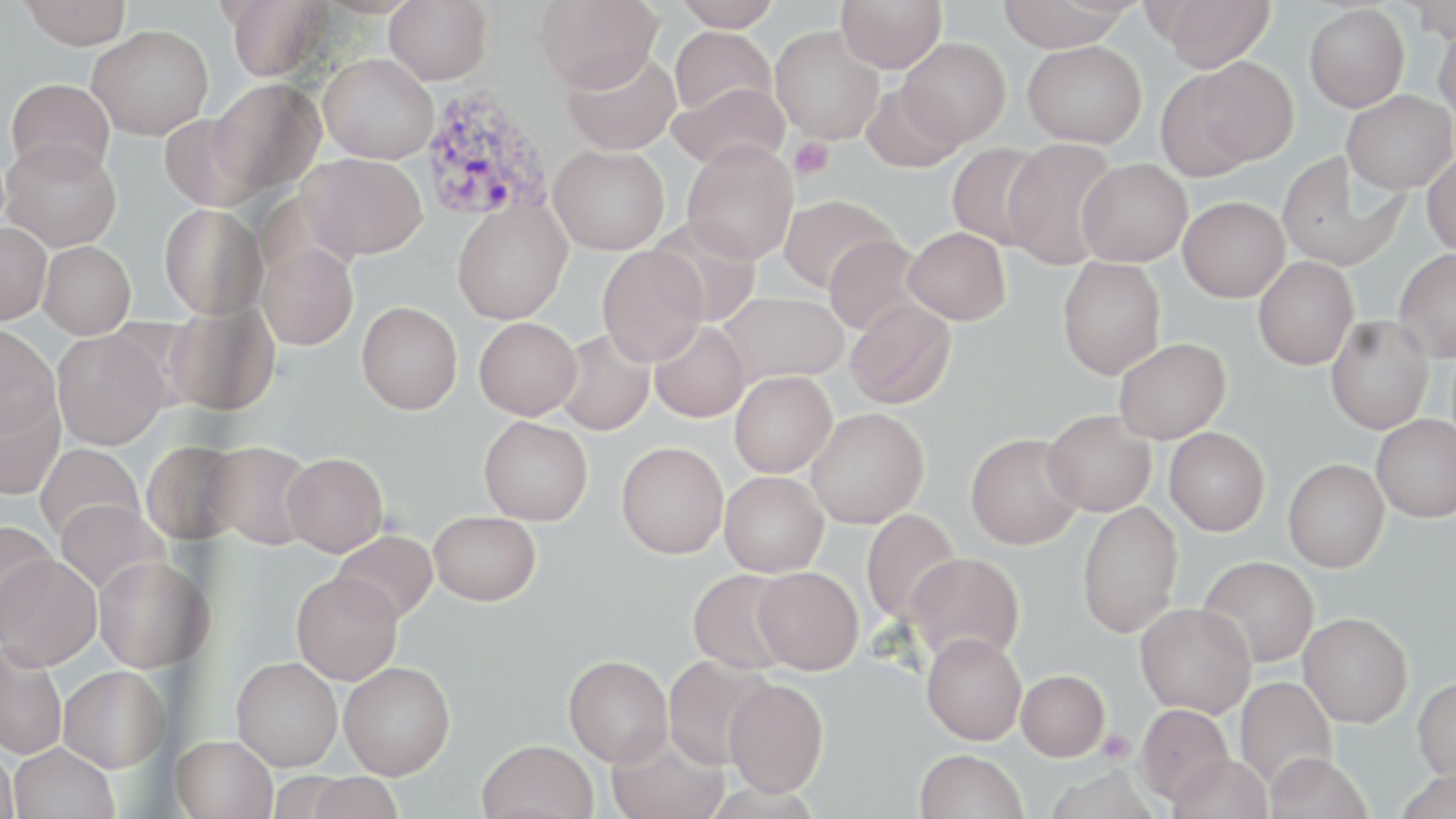
Summary:
  - Coordinate format: approximate bounding boxes as (x1,y1)-(x2,y2) corner pairs in pixels
  - Platelet locations: (788,138)-(834,179), (1097,730)-(1134,763)
  - Plasmodium vivax-infected red blood cell locations: (418,85)-(554,226)
  - Uninfected red blood cell locations: (20,0)-(133,49), (385,0)-(493,84), (534,0)-(662,93), (674,0)-(780,30), (836,0)-(946,73), (997,0)-(1132,52), (1157,0)-(1276,72), (1407,0)-(1456,42), (223,1)-(330,81), (1304,4)-(1409,111), (1434,22)-(1456,122), (87,25)-(213,139), (670,26)-(777,118), (770,26)-(884,145), (899,38)-(1011,146), (1023,40)-(1146,147), (562,49)-(681,155), (319,53)-(438,163), (1187,57)-(1299,166), (5,78)-(115,177), (208,79)-(325,195), (670,82)-(789,172), (861,83)-(963,172), (1342,91)-(1455,194), (159,114)-(262,211), (1,139)-(121,251), (1002,140)-(1120,268), (682,142)-(799,265), (947,143)-(1049,250), (549,145)-(670,254), (1422,151)-(1456,256), (1277,152)-(1406,271), (299,153)-(427,261), (1077,158)-(1193,266), (777,194)-(901,293), (1178,196)-(1290,302), (451,200)-(572,324), (158,204)-(267,320), (649,217)-(762,326), (0,222)-(51,324), (903,227)-(1011,324), (823,234)-(929,336), (38,241)-(135,338), (257,243)-(358,350), (597,246)-(709,366), (1394,248)-(1456,362), (1253,256)-(1358,370), (1057,257)-(1166,379), (717,292)-(849,385), (845,299)-(956,409), (165,300)-(280,415), (357,301)-(463,414), (1325,316)-(1433,434), (474,317)-(582,419), (649,320)-(750,422), (0,326)-(60,437), (554,329)-(654,436), (52,330)-(169,449), (1113,338)-(1230,443), (730,371)-(837,477), (0,394)-(65,500), (807,407)-(929,528), (1042,410)-(1156,516), (1371,414)-(1456,522), (479,416)-(593,525), (1165,428)-(1269,535), (966,433)-(1083,549), (141,440)-(246,545), (205,440)-(316,550), (616,442)-(728,558), (35,444)-(144,543), (282,452)-(388,556), (1283,459)-(1389,572), (719,471)-(829,577), (55,499)-(167,596), (1077,501)-(1183,638), (860,508)-(963,628), (429,511)-(541,605), (0,520)-(57,630), (331,531)-(437,624), (905,552)-(1025,665), (1,554)-(102,669), (1198,555)-(1319,667), (93,556)-(213,672), (752,566)-(864,675), (688,569)-(797,675), (291,572)-(403,684), (1135,603)-(1255,717), (1298,612)-(1412,727), (921,632)-(1027,745), (0,645)-(67,759), (564,655)-(673,766), (663,655)-(773,769), (232,656)-(342,771), (339,661)-(455,779), (59,665)-(170,772), (1016,670)-(1109,761), (1235,676)-(1337,790), (1413,676)-(1456,780), (723,678)-(829,796), (1136,703)-(1234,805), (606,732)-(729,819), (171,735)-(278,819), (477,739)-(599,819), (10,743)-(120,819), (0,745)-(19,818), (915,749)-(1028,819), (1265,752)-(1371,819), (1169,754)-(1274,819), (1394,768)-(1456,819), (301,773)-(405,819)
  - Slide-level diagnosis: Plasmodium vivax
  - Field of view: single
  - Modality: optical microscopy
  - Stain: May-Grünwald-Giemsa
  - Magnification: 1000x
  - Image size: 1456×819 pixels
  - Preparation: thin blood smear